Name the parasite shown.
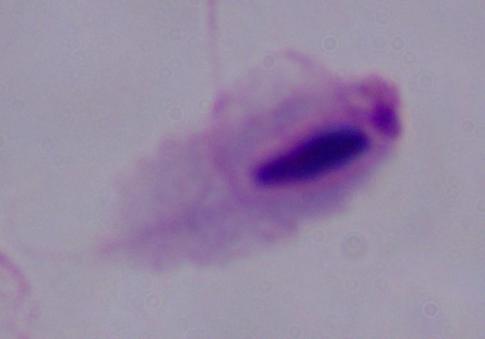

A trichomonad.

Captured at 1000x magnification. Micrograph.